Locate every Plasmodium parasite.
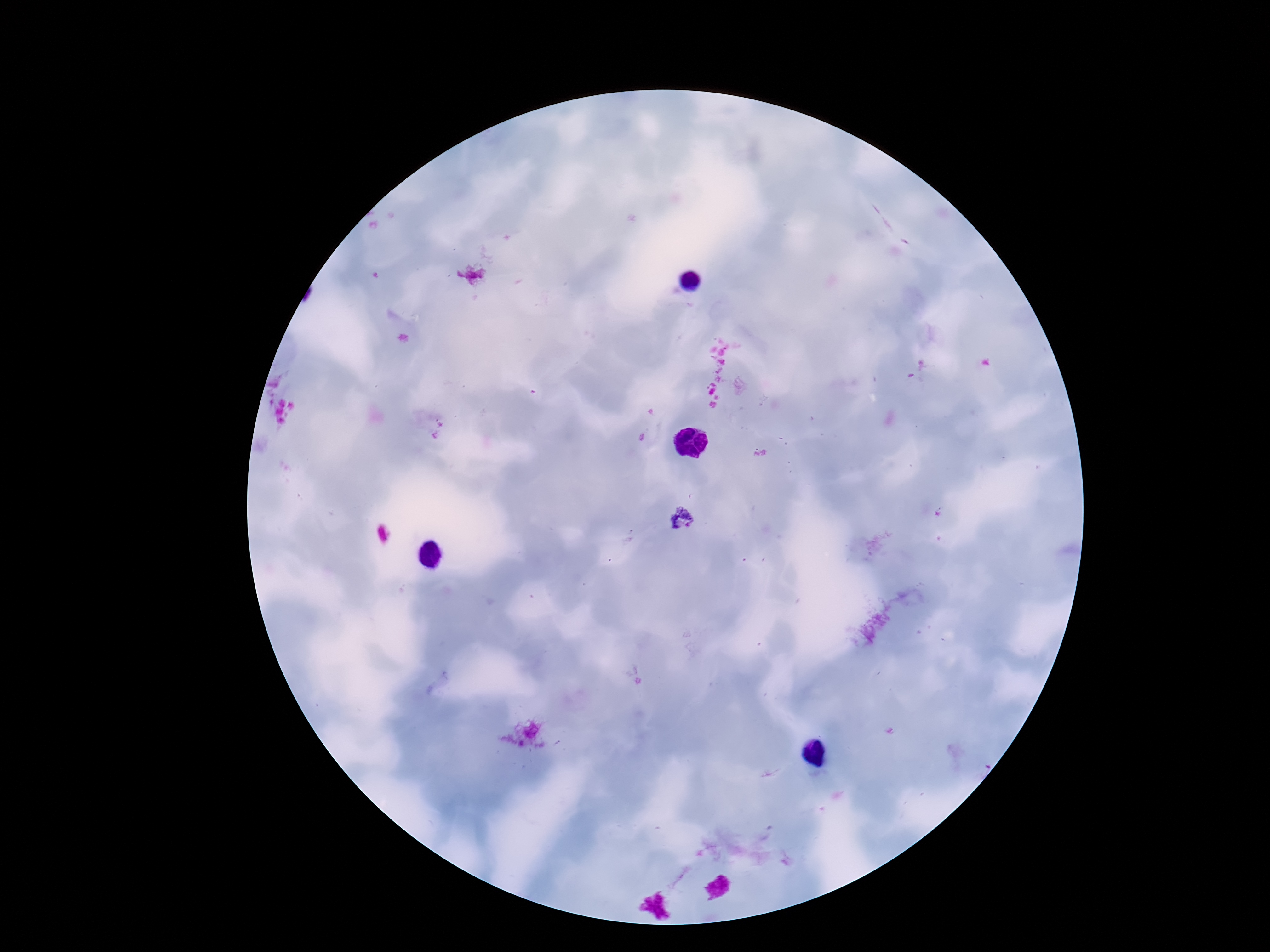

Approximate centers as (x, y) in pixels.
Plasmodium parasites: (683, 518).

Summary:
  - Magnification: 100x
  - Preparation: thick blood smear
  - Image size: 1270×952 pixels
  - Patient malaria status: positive
  - Stain: Giemsa
  - Capture: smartphone camera through the microscope eyepiece
  - Field of view: single